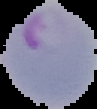

image size = 97×109 pixels
image type = segmented cell region with the area outside set to black
result = Plasmodium parasites identified
preparation = thin blood film